Report the malaria status of this cell.
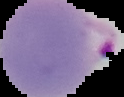

It is parasitized.

Summary:
  - Image size: 124×97 pixels
  - Image type: cell region segmented out of the field of view; surrounding area masked to black
  - Preparation: thin blood smear